Describe the morphology of the red blood cells.
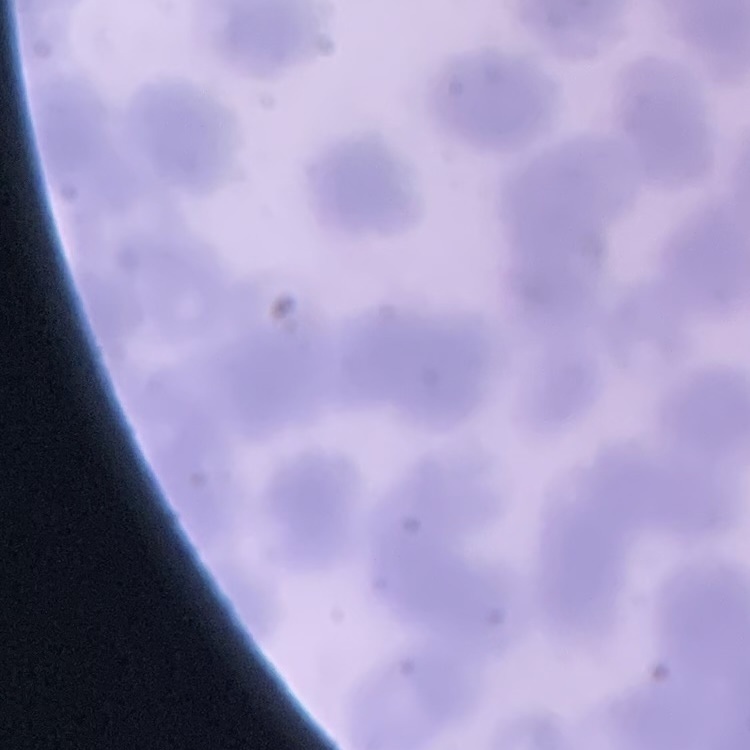
Rouleaux formation.

Summary:
  - Stain: Field's or Giemsa
  - Preparation: thin blood film
  - Image type: one tile cut from a larger photomicrograph